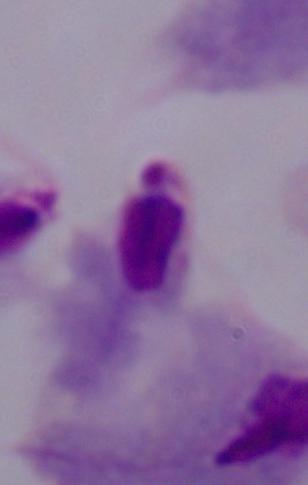

magnification = 1000x
modality = photomicrograph
identification = trichomonad